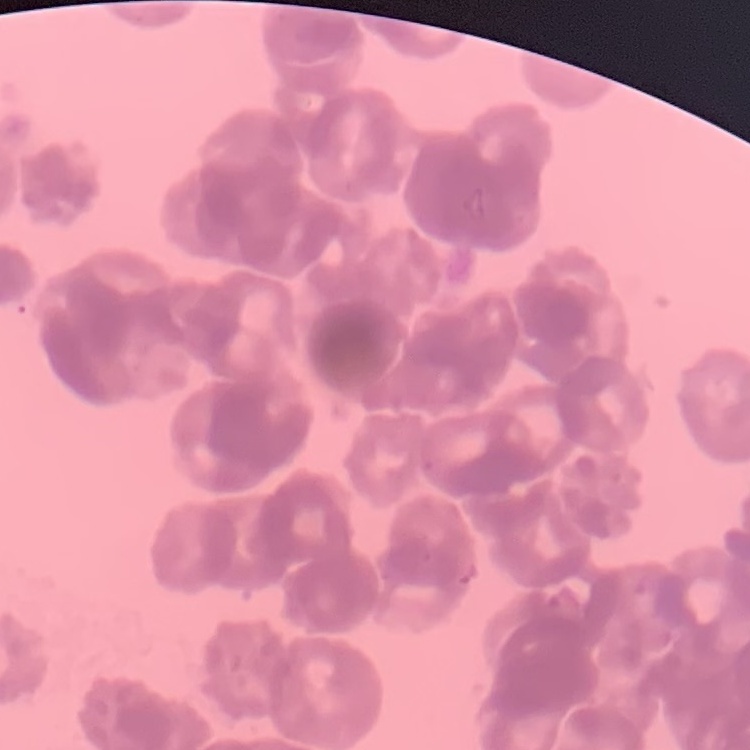 The erythrocytes show rouleaux formation. Square crop of a larger photomicrograph. Thin blood smear. Stained with either Field's or Giemsa.